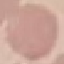
malaria status = uninfected
image type = cell patch, automatically extracted from a larger field of view and resized to 64 × 64 pixels
stain = Giemsa
preparation = thin blood film
capture = smartphone through the microscope eyepiece